Report the malaria status of this cell.
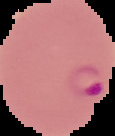
It is parasitized.

image type = segmented cell region on a black background
preparation = thin blood film
image size = 115×136 pixels